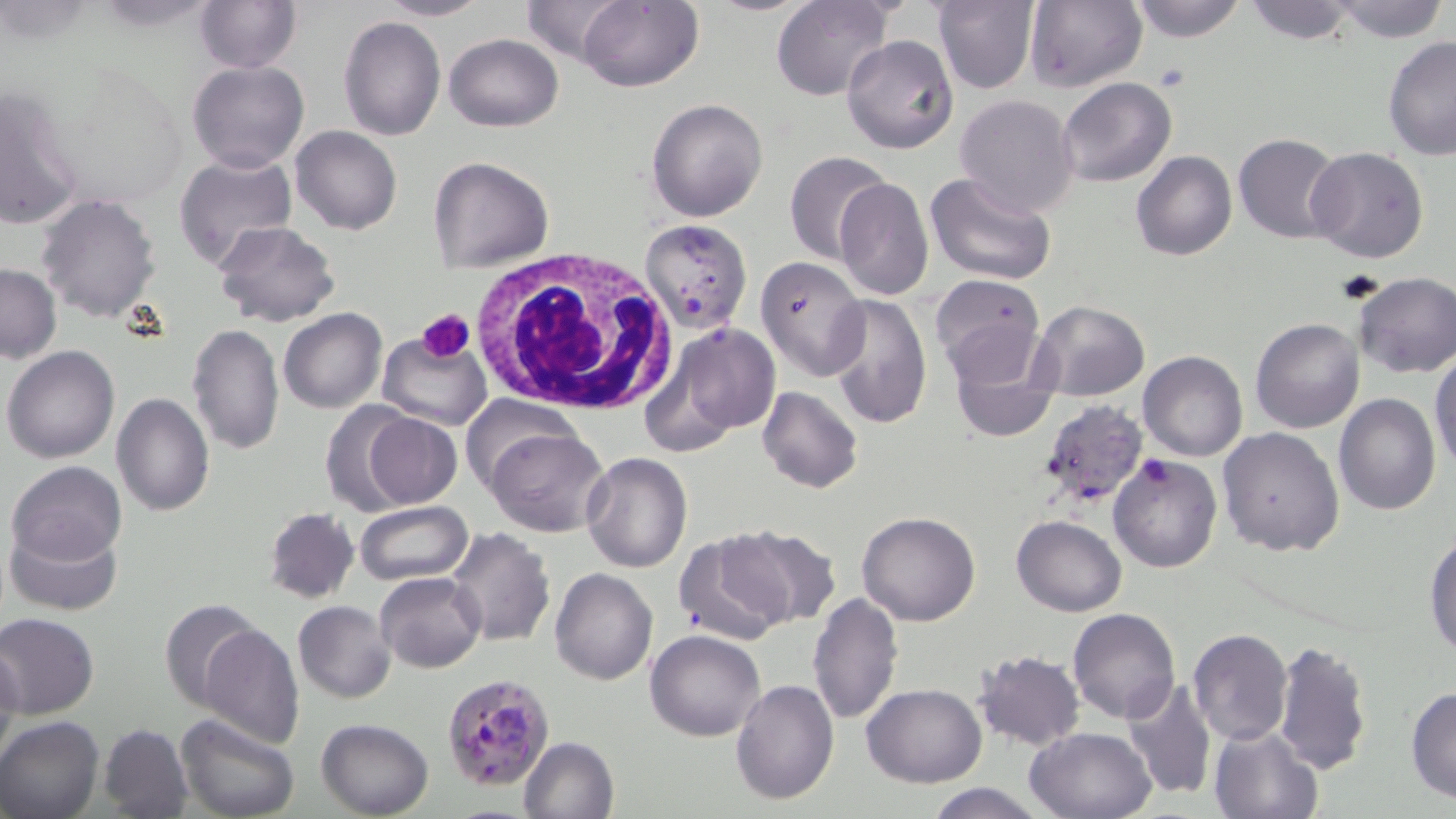
slide-level diagnosis = Plasmodium falciparum
white blood cell locations = approximate bounding boxes as [x1, y1, x2, y2] in pixels: [468, 251, 673, 414]
image size = 1456×819 pixels
field of view = one of a larger specimen
Plasmodium falciparum-infected red blood cell locations = approximate bounding boxes as [x1, y1, x2, y2] in pixels: [442, 671, 557, 791]
modality = light microscopy
magnification = 1000x
platelet locations = approximate bounding boxes as [x1, y1, x2, y2] in pixels: [418, 308, 476, 360]
preparation = thin blood film
uninfected red blood cell locations = approximate bounding boxes as [x1, y1, x2, y2] in pixels: [375, 0, 490, 21], [574, 0, 702, 91], [772, 0, 895, 101], [933, 0, 1039, 93], [1023, 0, 1147, 94], [1127, 0, 1251, 43], [1241, 0, 1361, 44], [194, 1, 303, 72], [520, 1, 632, 63], [1329, 1, 1452, 43], [339, 15, 445, 140], [444, 34, 563, 131], [842, 35, 959, 154], [1381, 35, 1456, 159], [187, 59, 309, 174], [1057, 77, 1176, 187], [0, 88, 85, 232], [954, 95, 1080, 218], [646, 97, 769, 222], [290, 126, 403, 234], [1233, 134, 1344, 242], [1306, 146, 1429, 265], [785, 150, 892, 263], [1132, 150, 1237, 261], [174, 153, 297, 270], [429, 156, 555, 273], [926, 171, 1059, 289], [833, 177, 932, 301], [36, 194, 161, 321], [641, 217, 753, 336], [212, 220, 339, 327], [755, 255, 871, 380], [0, 263, 60, 362], [1353, 272, 1456, 377], [929, 274, 1045, 385], [828, 294, 931, 431], [1025, 300, 1150, 401], [279, 309, 386, 412], [1250, 319, 1364, 434], [186, 323, 285, 456], [944, 323, 1060, 442], [653, 324, 780, 447], [377, 337, 491, 431], [3, 346, 119, 464], [1138, 350, 1247, 461], [1431, 351, 1456, 474], [757, 386, 863, 493], [112, 391, 215, 516], [1335, 392, 1440, 513], [459, 396, 577, 493], [1036, 398, 1150, 509], [316, 402, 423, 513], [361, 411, 461, 508], [1218, 427, 1345, 556], [484, 428, 610, 536], [580, 453, 693, 572], [1108, 455, 1223, 574], [6, 459, 128, 567], [353, 501, 472, 586], [263, 507, 360, 603], [857, 511, 981, 625], [1012, 515, 1126, 616], [2, 518, 123, 617], [725, 523, 841, 630], [446, 528, 554, 647], [671, 532, 789, 643], [1425, 533, 1456, 660], [550, 568, 658, 685], [376, 572, 485, 673], [808, 593, 902, 725], [158, 598, 263, 713], [293, 600, 395, 703], [1068, 609, 1180, 725], [0, 613, 100, 719], [197, 623, 305, 748], [1188, 628, 1292, 745], [644, 630, 766, 741], [1273, 640, 1373, 774], [0, 642, 22, 772], [972, 651, 1086, 750], [1121, 676, 1217, 802], [731, 679, 838, 805], [861, 683, 987, 785], [1405, 686, 1456, 803], [176, 713, 301, 819], [0, 715, 103, 819], [315, 718, 435, 817], [98, 723, 194, 818], [1208, 723, 1323, 819], [1025, 726, 1156, 818], [517, 736, 619, 819], [923, 782, 1046, 819]
stain = May-Grünwald-Giemsa